Identify the parasite.
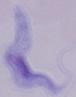

This is a trypanosome.

Summary:
  - Magnification: 1000x
  - Modality: micrograph